Assess the morphology of the erythrocytes.
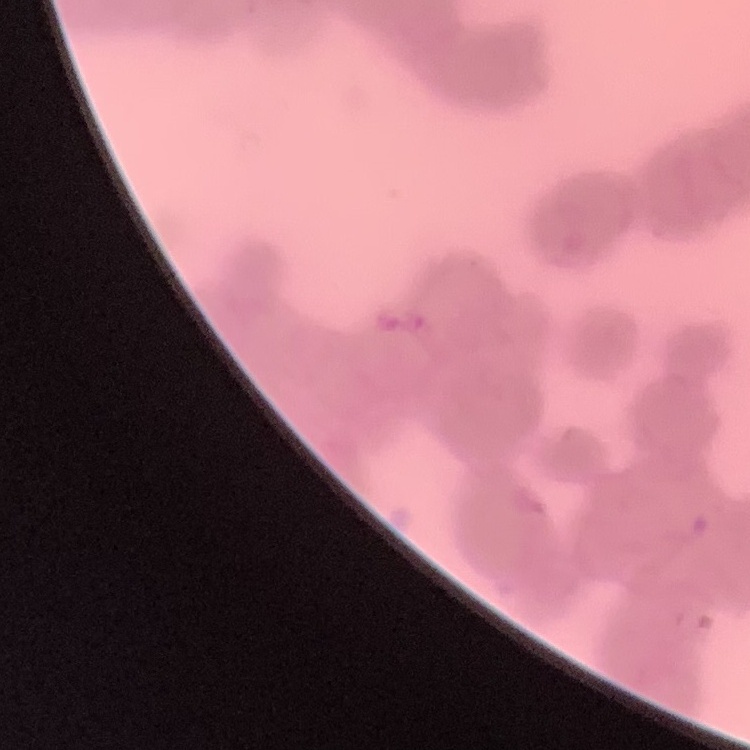
Rouleaux formation.

Summary:
  - Stain: Field's or Giemsa
  - Image type: square crop of a larger photomicrograph
  - Preparation: thin blood film